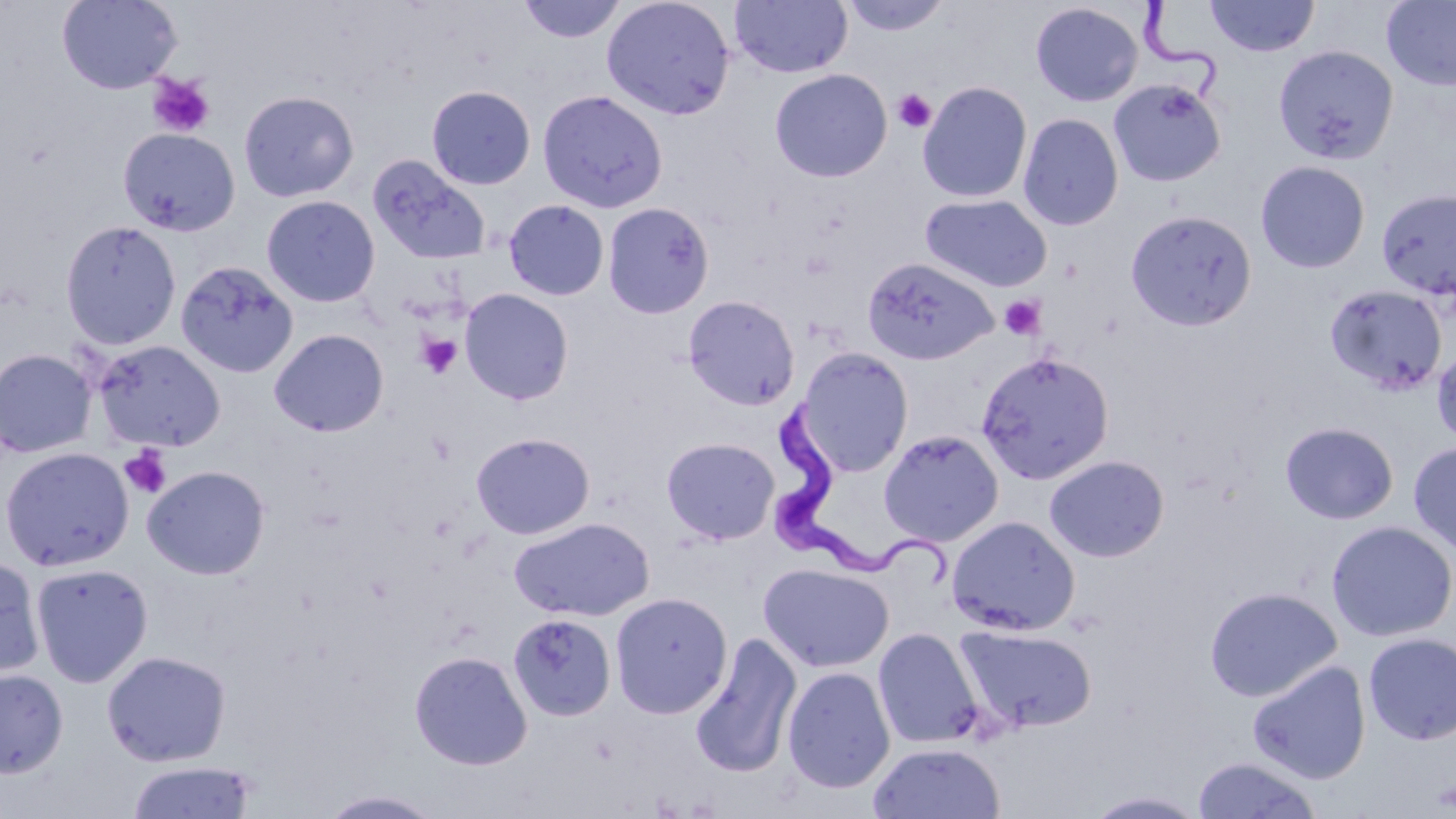 Approximate bounding boxes as named x1/y1/x2/y2 corners in pixels. Platelet locations: (x1=147, y1=73, x2=216, y2=138), (x1=892, y1=88, x2=936, y2=133), (x1=1000, y1=295, x2=1048, y2=341), (x1=417, y1=333, x2=462, y2=379), (x1=119, y1=446, x2=172, y2=499), (x1=1431, y1=778, x2=1456, y2=812). Uninfected red blood cell locations: (x1=56, y1=0, x2=183, y2=94), (x1=517, y1=0, x2=626, y2=44), (x1=601, y1=0, x2=736, y2=121), (x1=729, y1=0, x2=853, y2=79), (x1=839, y1=0, x2=953, y2=37), (x1=1204, y1=0, x2=1320, y2=58), (x1=1380, y1=1, x2=1456, y2=90), (x1=1030, y1=3, x2=1143, y2=107), (x1=1273, y1=44, x2=1399, y2=165), (x1=769, y1=69, x2=892, y2=183), (x1=1108, y1=78, x2=1227, y2=188), (x1=917, y1=81, x2=1032, y2=203), (x1=426, y1=85, x2=536, y2=190), (x1=536, y1=89, x2=669, y2=213), (x1=238, y1=90, x2=359, y2=203), (x1=1018, y1=113, x2=1123, y2=231), (x1=117, y1=128, x2=240, y2=237), (x1=368, y1=154, x2=492, y2=265), (x1=1255, y1=160, x2=1371, y2=273), (x1=1376, y1=188, x2=1456, y2=301), (x1=919, y1=193, x2=1053, y2=292), (x1=261, y1=195, x2=380, y2=308), (x1=504, y1=199, x2=609, y2=301), (x1=602, y1=202, x2=715, y2=319), (x1=1125, y1=209, x2=1257, y2=331), (x1=59, y1=220, x2=182, y2=351), (x1=862, y1=257, x2=1000, y2=366), (x1=176, y1=260, x2=299, y2=379), (x1=1324, y1=283, x2=1449, y2=395), (x1=459, y1=288, x2=574, y2=405), (x1=683, y1=295, x2=800, y2=410), (x1=268, y1=328, x2=389, y2=437), (x1=93, y1=340, x2=226, y2=452), (x1=1431, y1=345, x2=1456, y2=447), (x1=796, y1=347, x2=914, y2=476), (x1=0, y1=348, x2=97, y2=458), (x1=976, y1=350, x2=1114, y2=484), (x1=1280, y1=421, x2=1399, y2=524), (x1=879, y1=429, x2=1004, y2=547), (x1=470, y1=431, x2=596, y2=540), (x1=661, y1=436, x2=780, y2=545), (x1=1408, y1=442, x2=1456, y2=555), (x1=0, y1=446, x2=134, y2=571), (x1=1044, y1=454, x2=1170, y2=562), (x1=142, y1=465, x2=271, y2=580), (x1=946, y1=515, x2=1080, y2=636), (x1=508, y1=516, x2=655, y2=621), (x1=1326, y1=521, x2=1456, y2=642), (x1=0, y1=555, x2=45, y2=680), (x1=31, y1=563, x2=153, y2=687), (x1=758, y1=563, x2=894, y2=672), (x1=1204, y1=586, x2=1342, y2=702), (x1=610, y1=591, x2=732, y2=719), (x1=508, y1=613, x2=617, y2=721), (x1=954, y1=624, x2=1098, y2=734), (x1=872, y1=627, x2=985, y2=749), (x1=690, y1=632, x2=803, y2=779), (x1=1363, y1=633, x2=1456, y2=745), (x1=101, y1=650, x2=232, y2=767), (x1=409, y1=650, x2=533, y2=770), (x1=1247, y1=660, x2=1371, y2=784), (x1=782, y1=666, x2=895, y2=794), (x1=0, y1=668, x2=68, y2=778), (x1=868, y1=742, x2=1006, y2=819), (x1=1191, y1=755, x2=1322, y2=819), (x1=125, y1=760, x2=258, y2=819), (x1=316, y1=789, x2=447, y2=818), (x1=1083, y1=789, x2=1210, y2=818). Trypanosoma brucei locations: (x1=1136, y1=0, x2=1225, y2=104), (x1=776, y1=405, x2=953, y2=588). Slide-level diagnosis: Trypanosoma brucei. May-Grünwald-Giemsa stain. Optical microscopy. Single field of view. Image is 1456×819 pixels. Thin blood film. Captured at 1000x magnification.